Classify this cell by malaria status.
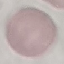
It is uninfected.

stain = Giemsa
capture = smartphone through the microscope eyepiece
preparation = thin blood smear
image type = cell patch, automatically extracted from a larger field of view and resized to 64 × 64 pixels